Assess this cell for malaria.
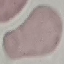

Uninfected.

capture = smartphone through the microscope eyepiece
stain = Giemsa
preparation = thin blood smear
image type = automatically extracted cell patch, resized to 64 × 64 pixels